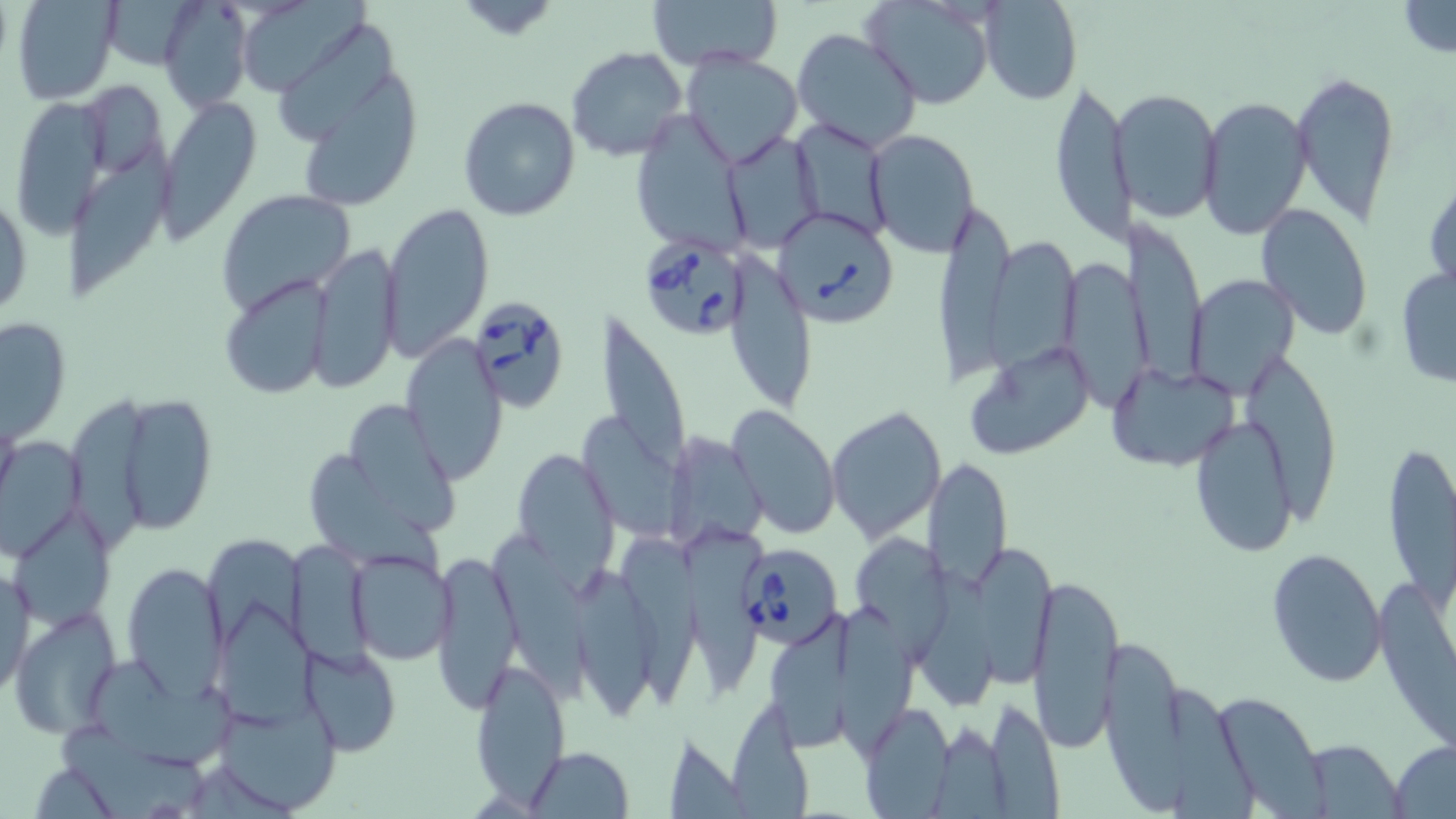

Approximate bounding boxes as [x1, y1, x2, y2] in pixels. Uninfected red blood cell locations: [9, 0, 120, 104], [233, 0, 373, 97], [647, 0, 785, 70], [863, 0, 995, 110], [158, 1, 252, 111], [979, 1, 1081, 107], [1396, 2, 1456, 56], [273, 23, 393, 139], [792, 28, 924, 153], [567, 47, 689, 163], [680, 51, 804, 170], [1292, 69, 1400, 227], [305, 77, 418, 206], [1049, 78, 1128, 250], [81, 80, 167, 181], [1118, 88, 1223, 223], [10, 95, 110, 243], [1197, 95, 1314, 239], [459, 97, 582, 222], [158, 98, 260, 234], [630, 113, 747, 253], [793, 118, 894, 239], [864, 128, 980, 258], [721, 130, 824, 256], [70, 151, 166, 296], [1424, 170, 1455, 303], [0, 188, 32, 325], [214, 188, 356, 314], [939, 197, 1019, 386], [380, 201, 495, 359], [1256, 204, 1374, 340], [1123, 221, 1214, 387], [309, 242, 404, 392], [991, 242, 1082, 370], [736, 250, 817, 412], [1057, 254, 1146, 408], [1393, 262, 1456, 389], [1188, 272, 1301, 400], [218, 275, 335, 401], [594, 309, 690, 481], [2, 315, 72, 444], [400, 334, 507, 485], [963, 339, 1098, 460], [1238, 342, 1341, 525], [1106, 361, 1241, 471], [69, 402, 158, 551], [126, 403, 213, 532], [351, 403, 464, 536], [727, 403, 840, 541], [826, 404, 947, 544], [1191, 416, 1295, 558], [582, 419, 693, 536], [662, 428, 770, 549], [0, 434, 88, 564], [1380, 434, 1455, 607], [510, 446, 620, 579], [307, 458, 445, 577], [925, 458, 1014, 595], [9, 506, 114, 631], [479, 523, 599, 698], [681, 528, 765, 694], [615, 533, 713, 708], [202, 535, 309, 645], [857, 536, 951, 665], [288, 537, 374, 673], [971, 544, 1061, 686], [350, 547, 456, 664], [431, 547, 523, 713], [1266, 547, 1387, 689], [1, 559, 34, 699], [121, 562, 228, 701], [1026, 571, 1124, 753], [580, 572, 657, 717], [838, 593, 917, 752], [214, 604, 314, 726], [8, 607, 119, 737], [769, 613, 859, 750], [1105, 639, 1193, 812], [301, 641, 401, 757], [469, 655, 571, 806], [92, 659, 242, 766], [1166, 682, 1257, 819], [1209, 691, 1328, 815], [212, 694, 344, 816], [985, 697, 1062, 816], [857, 702, 956, 816], [725, 705, 818, 819], [932, 719, 1010, 819], [60, 721, 206, 813], [661, 731, 748, 817], [1390, 738, 1456, 818], [1302, 739, 1403, 817], [525, 747, 634, 819], [28, 763, 121, 817]. Babesia divergens-infected red blood cell locations: [772, 206, 905, 328], [637, 235, 751, 340], [465, 295, 570, 411], [740, 554, 838, 646]. Slide-level diagnosis: Babesia divergens. One field of a larger specimen. May-Grünwald-Giemsa stain. Image is 1456×819 pixels. Light microscopy. 1000x magnification. Thin blood film.